State the preparation type.
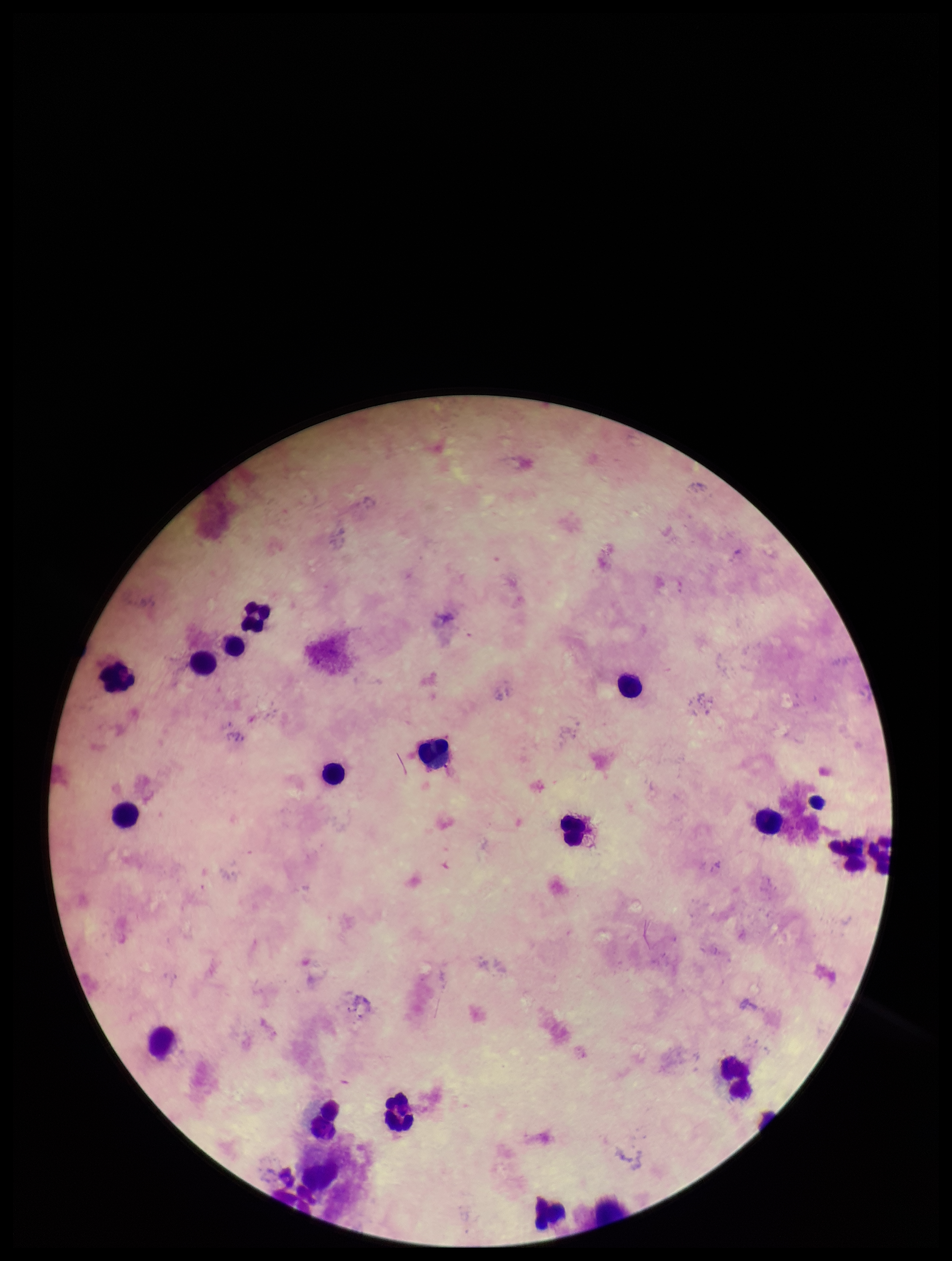

It is a thick blood smear.

{
  "capture": "smartphone photograph through the microscope eyepiece",
  "plasmodium_parasites": "none identified",
  "stain": "Giemsa",
  "field_of_view": "single",
  "leukocyte_count": 17,
  "patient_malaria_status": "negative",
  "image_size": "952×1261 pixels",
  "parasite_count": 0
}